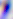
Summary:
  - Modality: micrograph
  - Identification: Toxoplasma gondii
  - Magnification: 400x